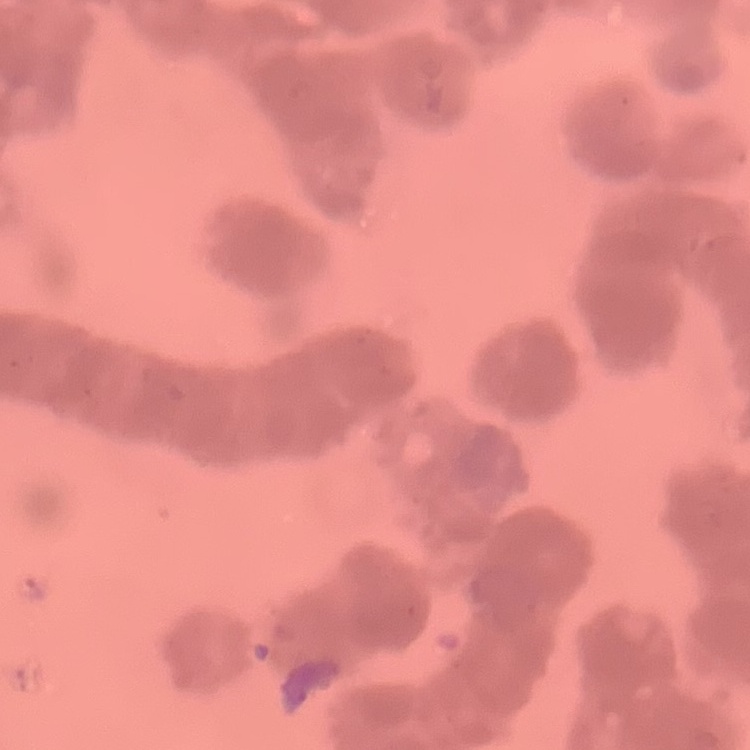 The erythrocytes exhibit rouleaux formation. Thin blood film. One tile cut from a larger photomicrograph. Stained with either Field's or Giemsa.